Assess the morphology of the erythrocytes.
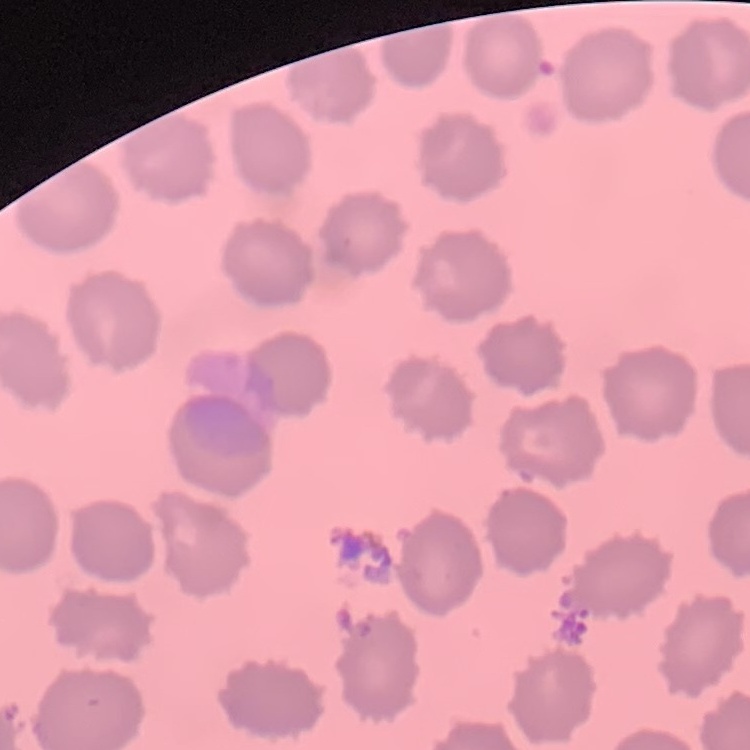

No rouleaux formation.

image_type: square crop of a larger photomicrograph
preparation: thin peripheral smear
stain: Field's or Giemsa